Identify the blood parasite species.
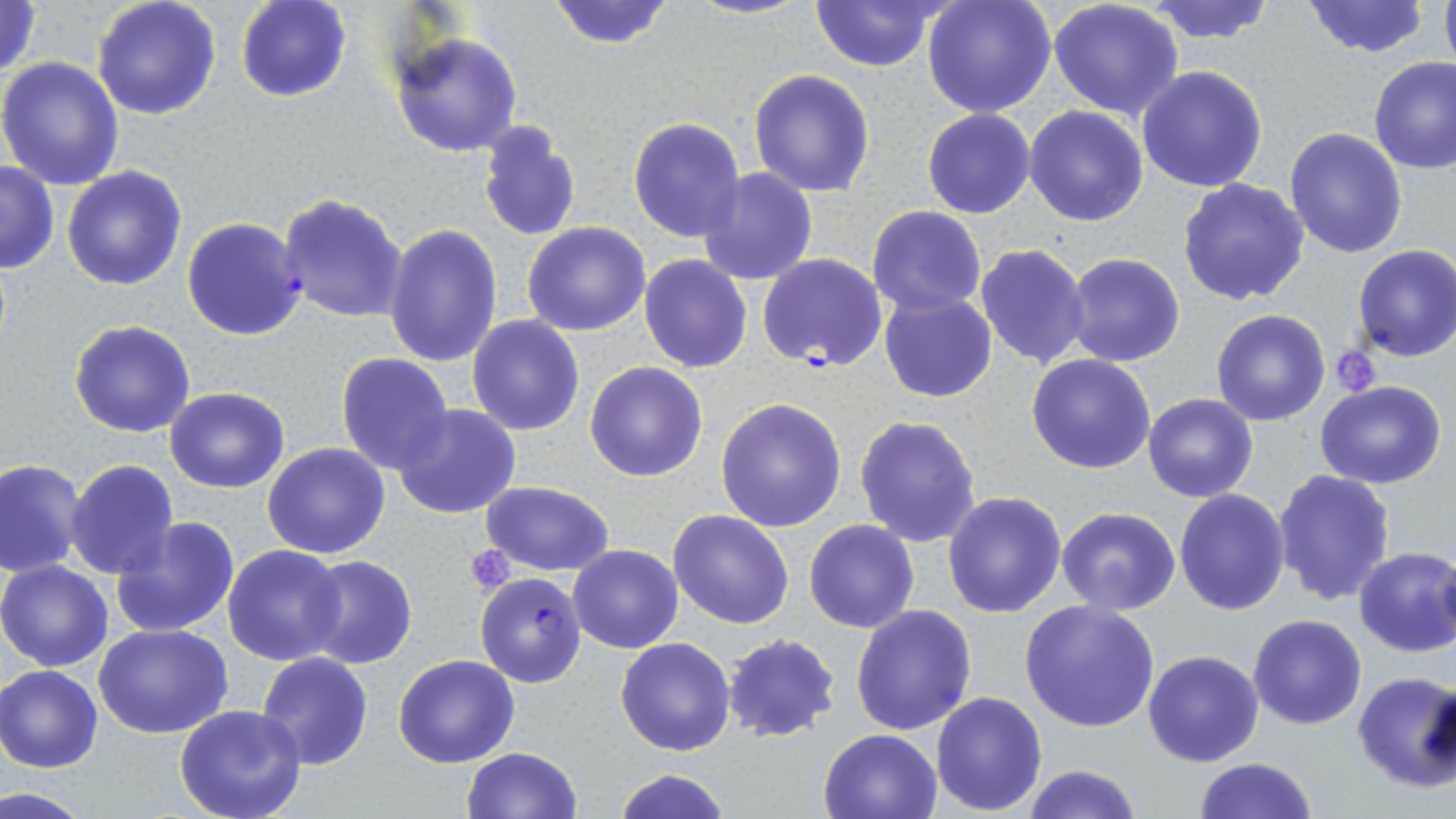
Plasmodium falciparum.

preparation = thin blood smear
magnification = 1000x
uninfected red blood cell locations = approximate bounding boxes as [x1, y1, x2, y2] in pixels: [0, 0, 43, 81], [92, 0, 221, 120], [236, 0, 351, 103], [547, 0, 676, 51], [685, 0, 814, 19], [923, 0, 1057, 119], [1047, 0, 1186, 120], [1299, 0, 1432, 58], [1439, 0, 1456, 72], [806, 1, 947, 71], [1142, 1, 1280, 45], [389, 30, 524, 157], [0, 56, 125, 191], [1369, 56, 1456, 174], [1137, 65, 1269, 193], [748, 69, 875, 195], [1024, 106, 1149, 227], [923, 110, 1034, 219], [628, 117, 745, 243], [476, 120, 583, 241], [1283, 127, 1407, 259], [0, 160, 60, 275], [62, 165, 187, 291], [696, 169, 818, 286], [1178, 178, 1310, 304], [277, 191, 409, 324], [866, 206, 986, 315], [522, 222, 650, 336], [385, 223, 503, 367], [973, 243, 1092, 369], [1352, 245, 1456, 362], [1063, 253, 1185, 368], [639, 254, 753, 373], [879, 291, 997, 403], [1210, 310, 1330, 427], [467, 314, 585, 436], [69, 320, 196, 438], [334, 353, 453, 473], [1027, 353, 1157, 474], [584, 361, 709, 482], [1315, 381, 1447, 489], [164, 388, 290, 493], [300, 391, 434, 537], [1143, 394, 1259, 502], [715, 398, 847, 532], [393, 403, 522, 520], [854, 413, 983, 547], [262, 442, 390, 559], [64, 458, 179, 580], [0, 459, 85, 574], [1272, 468, 1396, 607], [480, 481, 616, 577], [1174, 489, 1289, 614], [942, 491, 1067, 618], [1056, 507, 1181, 615], [668, 510, 794, 629], [110, 517, 241, 639], [804, 520, 920, 634], [568, 543, 684, 653], [223, 545, 348, 666], [1352, 546, 1456, 659], [300, 556, 417, 669], [0, 560, 115, 671], [1019, 600, 1160, 733], [850, 604, 978, 736], [1248, 614, 1366, 729], [1165, 620, 1330, 750], [94, 622, 234, 740], [722, 634, 840, 743], [615, 637, 739, 756], [1143, 650, 1264, 767], [255, 653, 374, 770], [394, 654, 520, 768], [0, 665, 103, 773], [1351, 671, 1456, 792], [931, 691, 1047, 813], [174, 705, 307, 819], [818, 727, 944, 819], [460, 747, 582, 819], [1193, 757, 1317, 819], [1020, 765, 1141, 819], [613, 767, 729, 819]
platelet locations = approximate bounding boxes as [x1, y1, x2, y2] in pixels: [1330, 344, 1383, 396], [465, 544, 515, 593]
image size = 1456×819 pixels
stain = May-Grünwald-Giemsa
modality = light microscopy
Plasmodium falciparum-infected red blood cell locations = approximate bounding boxes as [x1, y1, x2, y2] in pixels: [182, 217, 307, 340], [757, 253, 888, 372], [475, 573, 586, 687]
field of view = one of a larger specimen